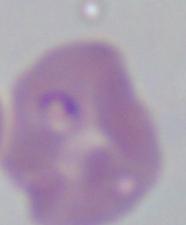 A Babesia parasite is shown. 1000x magnification. Micrograph.